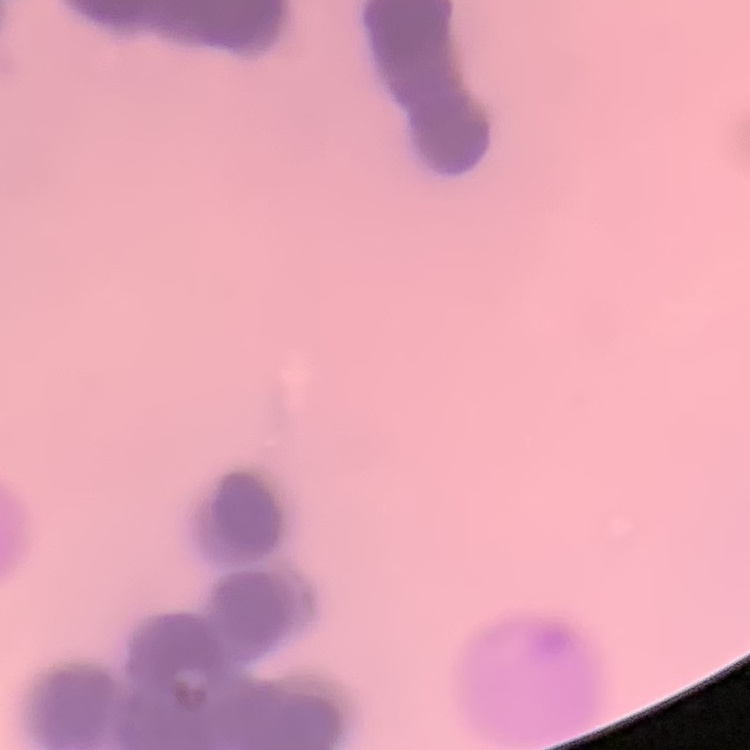
The erythrocytes exhibit rouleaux formation. Thin blood film. Stained with either Field's or Giemsa. One tile cut from a larger photomicrograph.